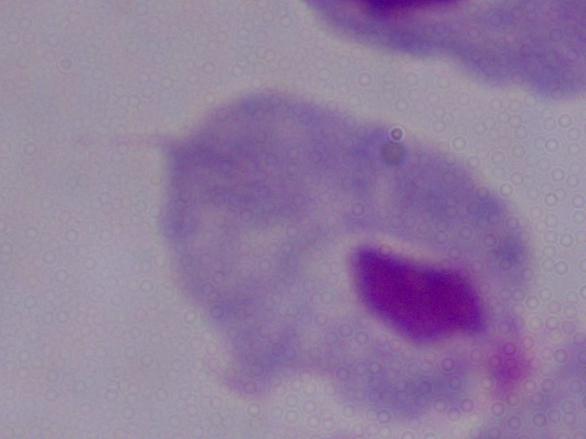

Summary:
  - Magnification: 1000x
  - Modality: photomicrograph
  - Identification: trichomonad